Name the blood parasite species.
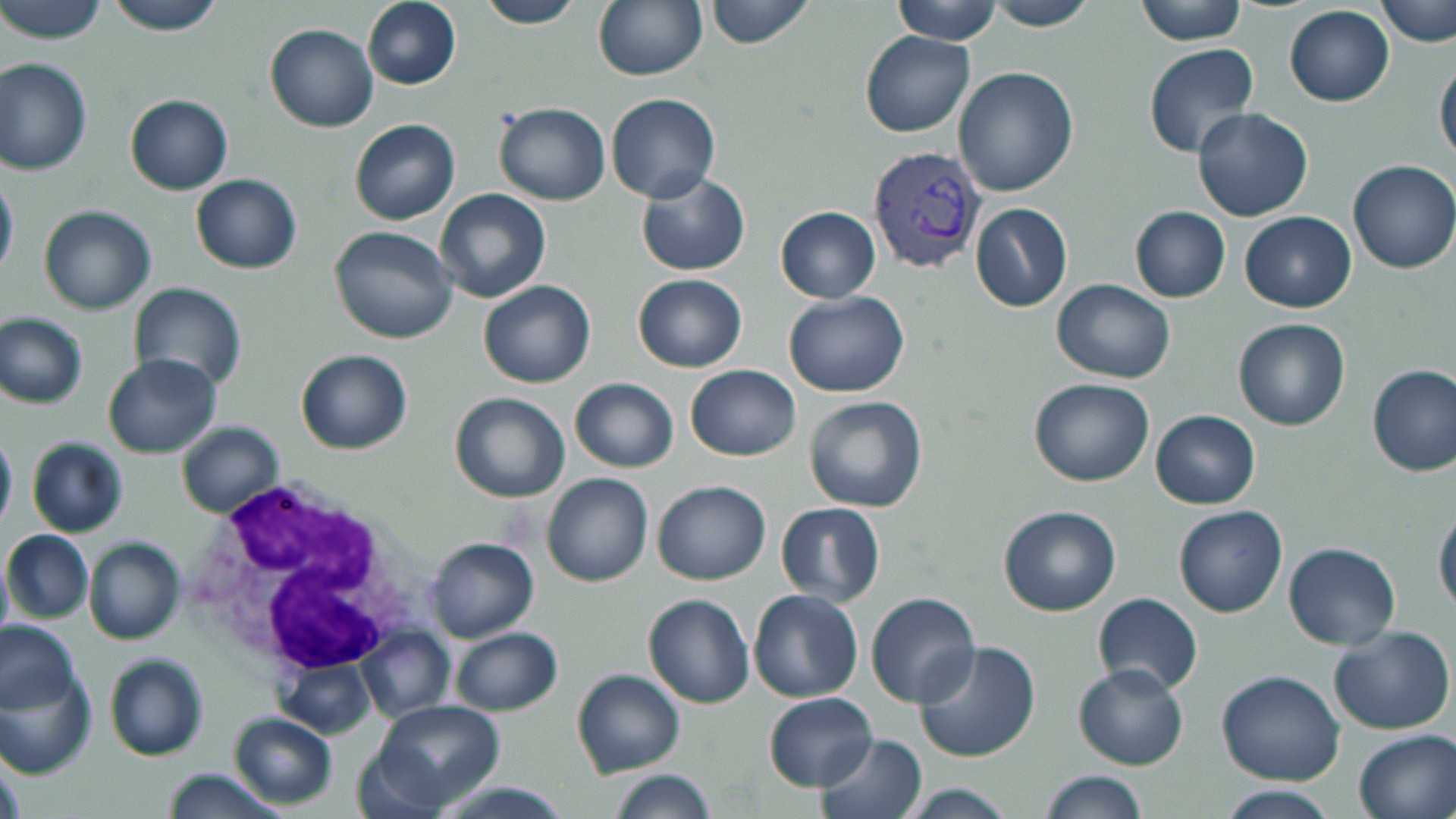

Plasmodium vivax.

Approximate bounding boxes as (x1, y1, x2, y2) in pixels. Plasmodium vivax-infected red blood cell locations: (868, 144, 987, 274). White blood cell locations: (183, 473, 414, 680). Uninfected red blood cell locations: (0, 0, 110, 44), (101, 0, 229, 35), (362, 0, 461, 90), (476, 0, 585, 28), (592, 0, 706, 81), (704, 0, 815, 48), (891, 0, 1005, 44), (1133, 0, 1251, 43), (1376, 0, 1454, 47), (984, 2, 1101, 31), (1284, 7, 1394, 105), (265, 23, 380, 131), (859, 31, 975, 136), (1144, 43, 1260, 157), (1435, 53, 1456, 164), (0, 58, 93, 175), (952, 65, 1078, 196), (606, 93, 720, 202), (124, 94, 233, 194), (493, 103, 610, 206), (1192, 106, 1312, 221), (351, 117, 460, 223), (1348, 159, 1456, 274), (635, 171, 750, 276), (0, 172, 18, 279), (191, 173, 303, 274), (436, 188, 551, 303), (970, 203, 1074, 312), (39, 205, 158, 316), (1129, 205, 1232, 302), (776, 206, 881, 302), (1240, 210, 1358, 311), (329, 225, 460, 344), (634, 273, 747, 372), (1052, 278, 1176, 382), (129, 281, 248, 393), (479, 281, 595, 387), (784, 293, 908, 396), (0, 311, 89, 408), (1234, 319, 1351, 431), (296, 350, 413, 454), (103, 355, 221, 459), (1367, 363, 1455, 475), (686, 365, 801, 461), (570, 377, 679, 472), (1029, 378, 1154, 487), (448, 390, 574, 504), (804, 395, 928, 512), (1151, 409, 1260, 509), (177, 421, 284, 517), (0, 429, 17, 530), (27, 437, 129, 537), (541, 472, 654, 587), (654, 479, 771, 584), (776, 503, 886, 606), (1432, 503, 1456, 619), (998, 505, 1122, 616), (1175, 506, 1287, 617), (3, 529, 93, 624), (86, 536, 185, 645), (426, 537, 539, 641), (1284, 541, 1400, 650), (0, 559, 12, 638), (749, 589, 863, 703), (866, 591, 981, 709), (1094, 592, 1202, 694), (644, 593, 753, 709), (0, 622, 81, 715), (1327, 624, 1455, 734), (358, 626, 456, 722), (450, 628, 564, 716), (914, 637, 1041, 762), (103, 653, 208, 761), (276, 655, 381, 740), (1075, 665, 1189, 768), (1217, 669, 1345, 785), (573, 670, 684, 777), (2, 672, 95, 776), (765, 693, 877, 790), (369, 700, 507, 812), (230, 712, 339, 809), (1354, 729, 1455, 819), (819, 733, 929, 819), (160, 766, 291, 818), (1039, 770, 1151, 819), (608, 771, 718, 819), (424, 778, 577, 819), (896, 784, 1020, 817), (1220, 788, 1341, 819). Single field of view. Optical microscopy. Image is 1456×819 pixels. Thin blood smear. May-Grünwald-Giemsa stain. Captured at 1000x magnification.